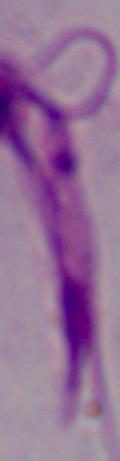
Summary:
  - Modality: photomicrograph
  - Magnification: 1000x
  - Identification: Leishmania